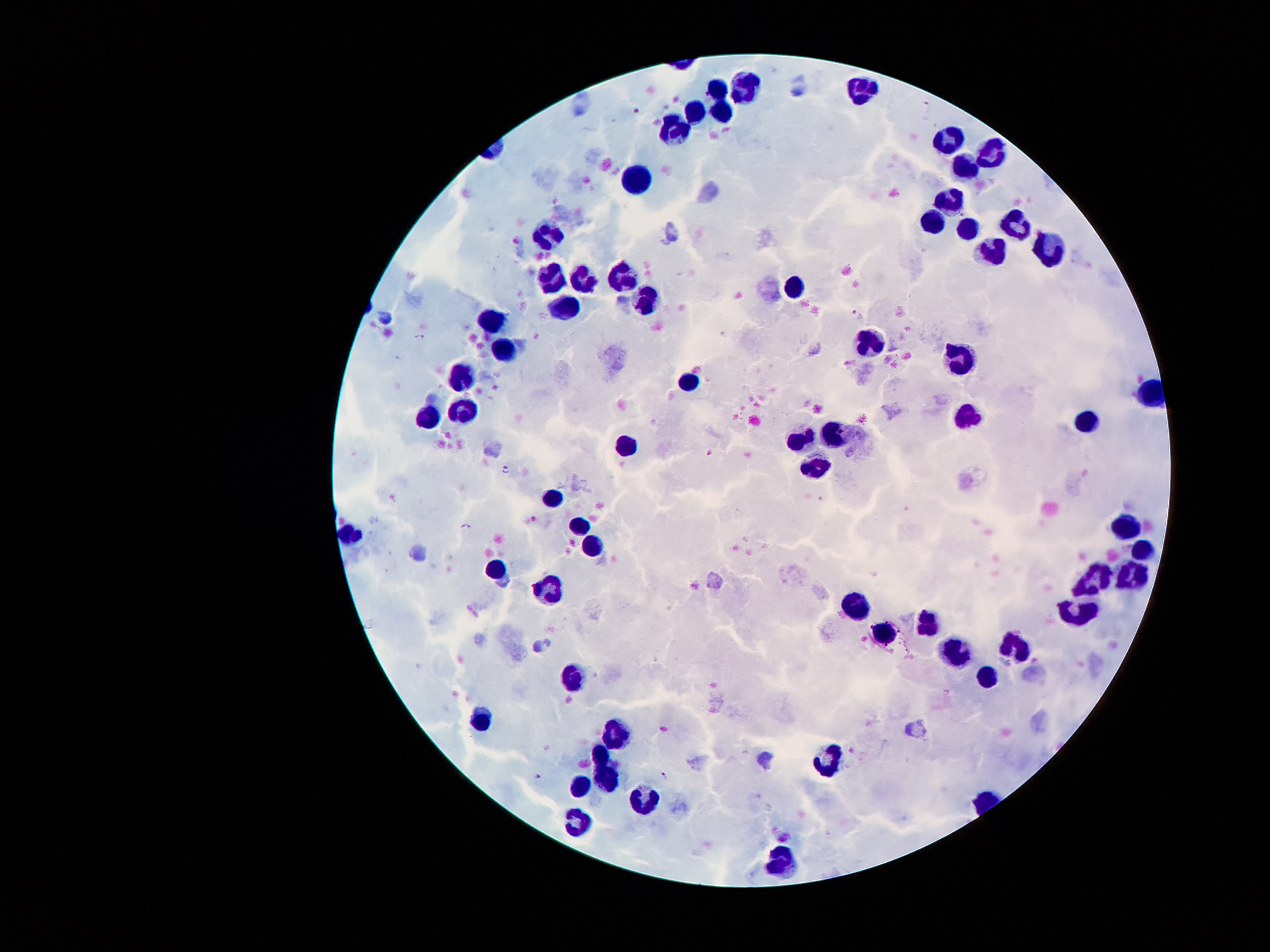

Approximate centers as (x, y) in pixels. Malaria parasite locations: (926, 104), (855, 314), (418, 337), (709, 452), (505, 468), (467, 527), (665, 775), (537, 776). Leukocyte locations: (746, 84), (717, 85), (862, 91), (696, 112), (721, 114), (671, 133), (950, 136), (990, 147), (963, 164), (637, 179), (951, 200), (927, 221), (1014, 221), (966, 227), (538, 231), (989, 252), (1047, 252), (551, 277), (580, 279), (616, 280), (791, 289), (651, 297), (566, 306), (490, 323), (874, 346), (507, 347), (964, 359), (459, 376), (689, 381), (463, 407), (427, 416), (969, 416), (1087, 422), (837, 433), (801, 440), (629, 445), (813, 463), (549, 496), (1123, 524), (572, 531), (351, 534), (595, 539), (1142, 549), (497, 571), (1095, 577), (1134, 578), (548, 590), (858, 602), (1075, 614), (928, 622), (883, 633), (1012, 648), (956, 656), (985, 678), (570, 680), (482, 721), (615, 734), (600, 753), (825, 757), (609, 775), (581, 783), (649, 796), (575, 823), (782, 857). Patient malaria status: positive for Plasmodium falciparum. Giemsa stain. Single field of view. 100x magnification. Thick peripheral-blood smear. Photographed through the microscope eyepiece with a smartphone camera. Image is 1270×952 pixels.